Classify this cell by malaria status.
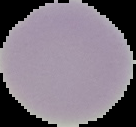
It is uninfected.

From a thin blood film. Image is 136×127 pixels. Segmented cell region on a black background.